Locate every blood parasite and identify its species.
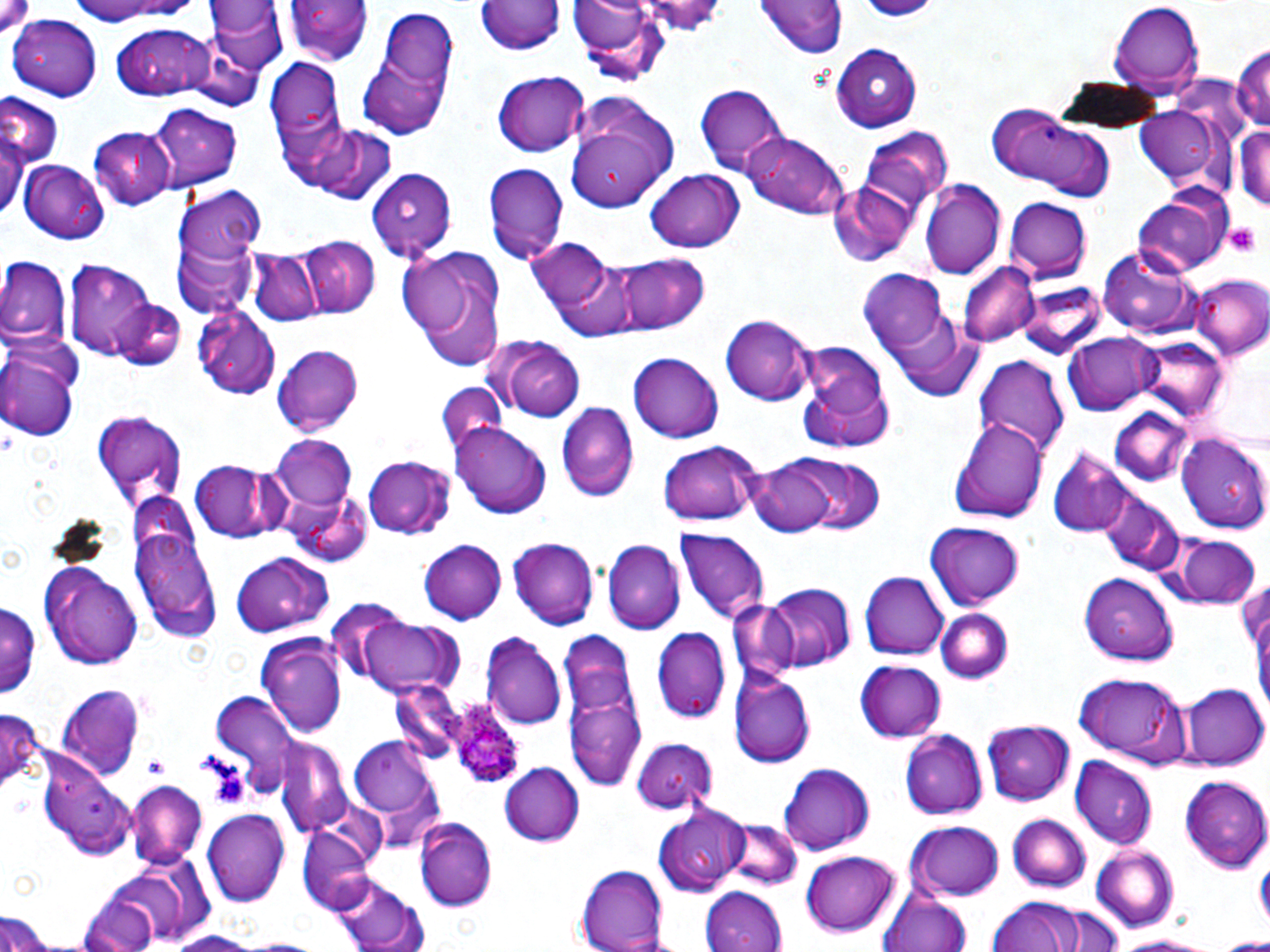

Approximate bounding boxes as named x1/y1/x2/y2 corners in pixels.
Plasmodium ovale-infected red blood cells: (x1=447, y1=696, x2=526, y2=790).
No Plasmodium falciparum, Plasmodium malariae, Plasmodium vivax, Babesia divergens, or Trypanosoma brucei observed.

Summary:
  - Platelet locations: (x1=1225, y1=221, x2=1261, y2=257), (x1=192, y1=748, x2=243, y2=787), (x1=144, y1=757, x2=170, y2=776), (x1=208, y1=760, x2=253, y2=809), (x1=1256, y1=857, x2=1270, y2=915)
  - Uninfected red blood cell locations: (x1=287, y1=0, x2=372, y2=67), (x1=568, y1=0, x2=669, y2=84), (x1=476, y1=1, x2=565, y2=58), (x1=760, y1=1, x2=846, y2=60), (x1=72, y1=2, x2=196, y2=30), (x1=206, y1=2, x2=288, y2=76), (x1=1108, y1=3, x2=1203, y2=97), (x1=358, y1=11, x2=457, y2=131), (x1=10, y1=16, x2=101, y2=99), (x1=111, y1=25, x2=216, y2=98), (x1=184, y1=39, x2=266, y2=110), (x1=1233, y1=41, x2=1270, y2=138), (x1=832, y1=44, x2=923, y2=132), (x1=267, y1=56, x2=349, y2=179), (x1=491, y1=71, x2=591, y2=157), (x1=693, y1=82, x2=788, y2=173), (x1=566, y1=92, x2=680, y2=209), (x1=0, y1=94, x2=61, y2=169), (x1=564, y1=98, x2=678, y2=210), (x1=150, y1=103, x2=241, y2=192), (x1=986, y1=103, x2=1118, y2=202), (x1=1134, y1=104, x2=1224, y2=192), (x1=1234, y1=120, x2=1270, y2=215), (x1=0, y1=124, x2=25, y2=219), (x1=297, y1=124, x2=397, y2=203), (x1=90, y1=127, x2=174, y2=210), (x1=863, y1=128, x2=954, y2=210), (x1=741, y1=130, x2=851, y2=220), (x1=19, y1=161, x2=109, y2=244), (x1=483, y1=161, x2=569, y2=266), (x1=366, y1=168, x2=455, y2=257), (x1=642, y1=168, x2=746, y2=253), (x1=920, y1=178, x2=1005, y2=277), (x1=827, y1=180, x2=914, y2=267), (x1=176, y1=188, x2=267, y2=293), (x1=1134, y1=194, x2=1231, y2=276), (x1=1003, y1=197, x2=1092, y2=283), (x1=171, y1=232, x2=260, y2=319), (x1=299, y1=234, x2=378, y2=318), (x1=529, y1=238, x2=625, y2=328), (x1=394, y1=246, x2=509, y2=368), (x1=1097, y1=246, x2=1202, y2=340), (x1=246, y1=248, x2=319, y2=325), (x1=615, y1=253, x2=710, y2=334), (x1=553, y1=256, x2=659, y2=339), (x1=0, y1=257, x2=70, y2=351), (x1=67, y1=263, x2=161, y2=358), (x1=959, y1=263, x2=1037, y2=346), (x1=858, y1=267, x2=955, y2=371), (x1=1187, y1=272, x2=1270, y2=359), (x1=1018, y1=278, x2=1108, y2=357), (x1=113, y1=300, x2=186, y2=372), (x1=193, y1=306, x2=281, y2=399), (x1=721, y1=313, x2=816, y2=405), (x1=887, y1=315, x2=985, y2=401), (x1=1062, y1=331, x2=1159, y2=415), (x1=487, y1=335, x2=586, y2=422), (x1=1136, y1=337, x2=1226, y2=421), (x1=795, y1=339, x2=897, y2=454), (x1=0, y1=344, x2=81, y2=442), (x1=273, y1=344, x2=365, y2=434), (x1=629, y1=351, x2=723, y2=442), (x1=975, y1=355, x2=1070, y2=462), (x1=438, y1=381, x2=504, y2=458), (x1=556, y1=405, x2=638, y2=501), (x1=1108, y1=406, x2=1193, y2=483), (x1=91, y1=409, x2=187, y2=504), (x1=950, y1=418, x2=1051, y2=522), (x1=452, y1=424, x2=551, y2=518), (x1=1176, y1=429, x2=1270, y2=533), (x1=268, y1=432, x2=355, y2=517), (x1=660, y1=441, x2=763, y2=528), (x1=1049, y1=451, x2=1130, y2=535), (x1=364, y1=454, x2=456, y2=539), (x1=795, y1=456, x2=885, y2=536), (x1=188, y1=460, x2=282, y2=542), (x1=749, y1=460, x2=837, y2=535), (x1=284, y1=492, x2=372, y2=567), (x1=1102, y1=495, x2=1184, y2=575), (x1=130, y1=518, x2=219, y2=640), (x1=924, y1=522, x2=1024, y2=609), (x1=676, y1=529, x2=769, y2=623), (x1=1175, y1=536, x2=1262, y2=608), (x1=509, y1=538, x2=598, y2=629), (x1=603, y1=539, x2=684, y2=633), (x1=421, y1=540, x2=508, y2=624), (x1=231, y1=550, x2=332, y2=637), (x1=39, y1=562, x2=144, y2=670), (x1=862, y1=572, x2=948, y2=660), (x1=1081, y1=575, x2=1182, y2=668), (x1=1237, y1=577, x2=1269, y2=667), (x1=758, y1=584, x2=855, y2=672), (x1=0, y1=594, x2=40, y2=704), (x1=325, y1=601, x2=417, y2=686), (x1=730, y1=601, x2=801, y2=682), (x1=935, y1=607, x2=1015, y2=685), (x1=354, y1=616, x2=469, y2=699), (x1=652, y1=628, x2=731, y2=724), (x1=483, y1=631, x2=566, y2=727), (x1=258, y1=634, x2=346, y2=736), (x1=560, y1=639, x2=645, y2=797), (x1=855, y1=661, x2=945, y2=742), (x1=730, y1=670, x2=815, y2=768), (x1=1073, y1=673, x2=1192, y2=767), (x1=392, y1=680, x2=464, y2=765), (x1=55, y1=681, x2=147, y2=780), (x1=1180, y1=683, x2=1267, y2=770), (x1=208, y1=690, x2=301, y2=795), (x1=0, y1=708, x2=45, y2=793), (x1=984, y1=720, x2=1075, y2=805), (x1=899, y1=729, x2=988, y2=818), (x1=349, y1=735, x2=445, y2=839), (x1=629, y1=735, x2=721, y2=814), (x1=275, y1=739, x2=353, y2=835), (x1=37, y1=751, x2=135, y2=857), (x1=1072, y1=756, x2=1157, y2=848), (x1=499, y1=762, x2=585, y2=843), (x1=777, y1=763, x2=876, y2=854), (x1=1179, y1=775, x2=1270, y2=872), (x1=125, y1=780, x2=207, y2=867), (x1=201, y1=808, x2=289, y2=904), (x1=654, y1=809, x2=749, y2=894), (x1=1007, y1=813, x2=1091, y2=891), (x1=415, y1=818, x2=497, y2=908), (x1=724, y1=819, x2=802, y2=890), (x1=906, y1=822, x2=1006, y2=900), (x1=299, y1=823, x2=378, y2=913), (x1=1090, y1=844, x2=1180, y2=931), (x1=800, y1=852, x2=901, y2=938), (x1=106, y1=855, x2=216, y2=943), (x1=577, y1=864, x2=671, y2=952), (x1=330, y1=874, x2=431, y2=950), (x1=703, y1=886, x2=789, y2=952), (x1=81, y1=889, x2=161, y2=952), (x1=878, y1=891, x2=975, y2=952), (x1=988, y1=898, x2=1090, y2=951), (x1=0, y1=913, x2=62, y2=948), (x1=159, y1=929, x2=267, y2=951), (x1=1109, y1=933, x2=1223, y2=951), (x1=1220, y1=936, x2=1270, y2=950)
  - Slide-level diagnosis: Plasmodium ovale
  - Stain: May-Grünwald-Giemsa
  - Field of view: single
  - Preparation: thin blood film
  - Image size: 1270×952 pixels
  - Modality: light microscopy
  - Magnification: 1000x